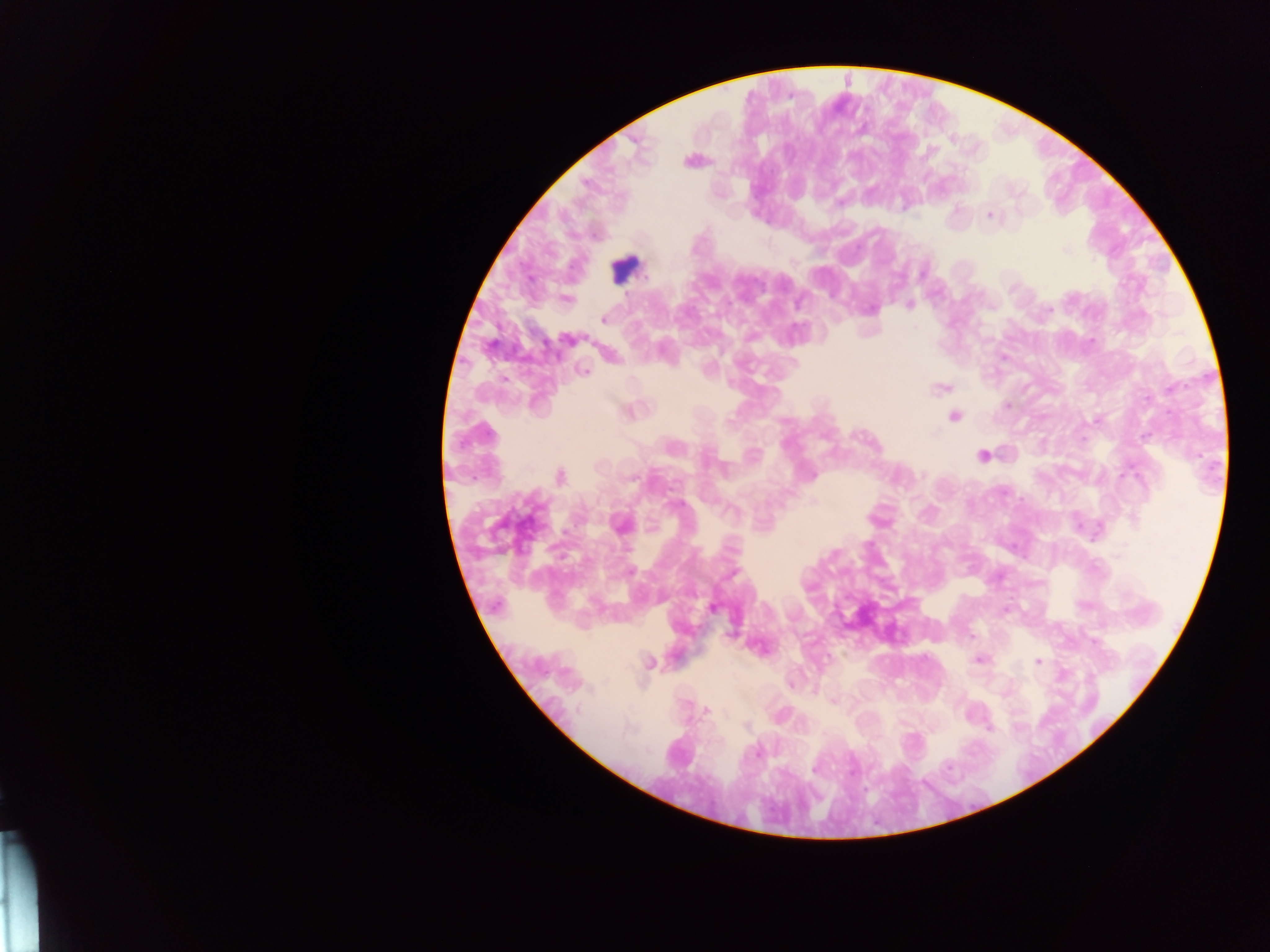
image_size: 1270×952 pixels
leukocyte_locations: 'approximate centers as {x, y} in pixels: {625, 268}'
field_of_view: single
preparation: thick blood smear
country: Ghana
capture: mobile-phone photograph through a microscope
malaria_parasite_locations: 'approximate centers as {x, y} in pixels: {989, 215}, {1065, 251}, {1094, 259}, {910, 305}, {870, 309}, {1049, 310}, {603, 319}, {915, 327}, {568, 340}, {1092, 340}, {584, 371}, {941, 388}, {1007, 405}, {954, 416}, {1096, 420}, {982, 456}, {923, 476}, {560, 477}, {634, 478}, {620, 524}, {834, 554}, {630, 571}, {732, 574}, {714, 609}, {1005, 610}, {980, 660}, {1037, 662}, {650, 663}, {832, 701}, {706, 710}, {990, 729}, {629, 730}, {758, 752}, {814, 769}'